Outline each blood parasite and name the species.
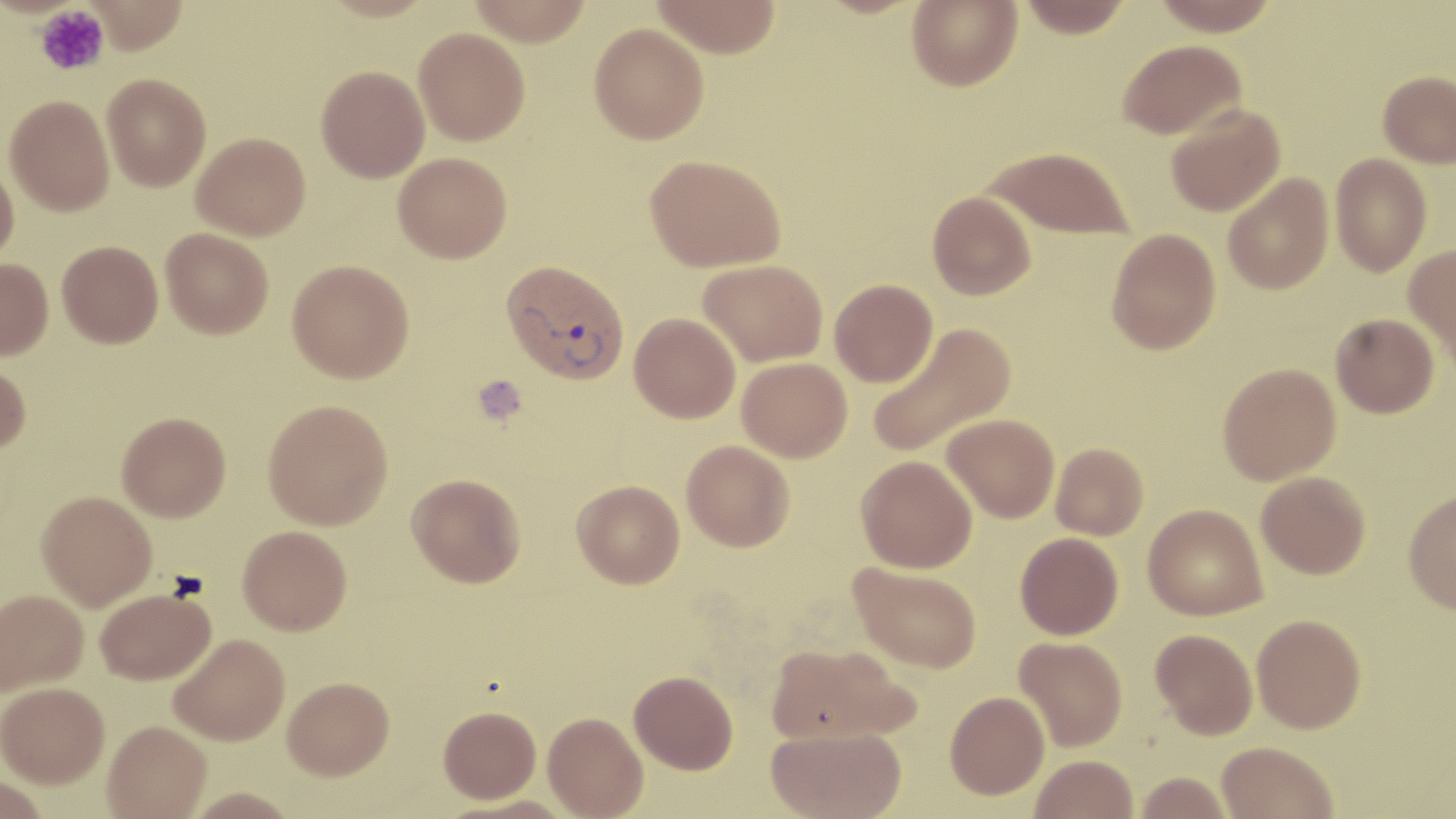

Approximate bounding boxes as (x1, y1, x2, y2) in pixels.
Plasmodium vivax-infected red blood cells: (501, 260, 630, 384).
No Plasmodium falciparum, Plasmodium ovale, Plasmodium malariae, Babesia divergens, or Trypanosoma brucei observed.

Uninfected red blood cell locations: (85, 0, 189, 54), (467, 0, 593, 45), (652, 0, 781, 58), (907, 0, 1022, 91), (1018, 0, 1132, 38), (1152, 0, 1280, 36), (589, 22, 708, 143), (414, 27, 530, 145), (1118, 39, 1247, 140), (316, 65, 430, 182), (1378, 70, 1456, 167), (102, 73, 211, 191), (5, 95, 114, 216), (1165, 104, 1285, 217), (191, 132, 311, 240), (983, 146, 1134, 239), (393, 152, 512, 263), (1330, 153, 1432, 276), (645, 154, 786, 271), (0, 162, 19, 265), (1223, 173, 1333, 295), (928, 191, 1036, 300), (161, 227, 274, 339), (1106, 228, 1221, 355), (56, 240, 163, 348), (1403, 243, 1456, 365), (0, 258, 53, 361), (287, 259, 414, 383), (699, 259, 828, 366), (830, 278, 938, 387), (629, 312, 740, 422), (1331, 313, 1439, 418), (867, 321, 1016, 460), (737, 357, 852, 462), (0, 361, 31, 455), (1218, 362, 1341, 485), (263, 399, 393, 530), (117, 412, 231, 521), (942, 413, 1060, 522), (682, 440, 795, 552), (1051, 443, 1149, 540), (856, 456, 978, 573), (1256, 471, 1371, 579), (407, 473, 526, 587), (571, 479, 685, 588), (36, 490, 157, 609), (1403, 490, 1456, 614), (1143, 504, 1267, 620), (238, 525, 352, 634), (1015, 532, 1123, 639), (848, 561, 983, 673), (0, 588, 88, 695), (95, 588, 215, 685), (1252, 613, 1366, 733), (1150, 629, 1258, 739), (169, 634, 290, 745), (1014, 636, 1127, 751), (766, 643, 916, 745), (629, 670, 738, 774), (282, 676, 394, 779), (0, 681, 109, 787), (945, 691, 1049, 799), (438, 705, 541, 803), (543, 711, 649, 818), (102, 720, 211, 819), (766, 726, 906, 819), (1216, 741, 1339, 819), (1030, 754, 1139, 819), (1134, 772, 1233, 818), (0, 775, 51, 819), (449, 795, 578, 819). Platelet locations: (35, 4, 109, 76), (473, 375, 528, 425). Slide-level diagnosis: Plasmodium vivax. May-Grünwald-Giemsa-stained preparation. 1000x magnification. Single field of view. Optical microscopy. Thin blood smear. Image is 1456×819 pixels.